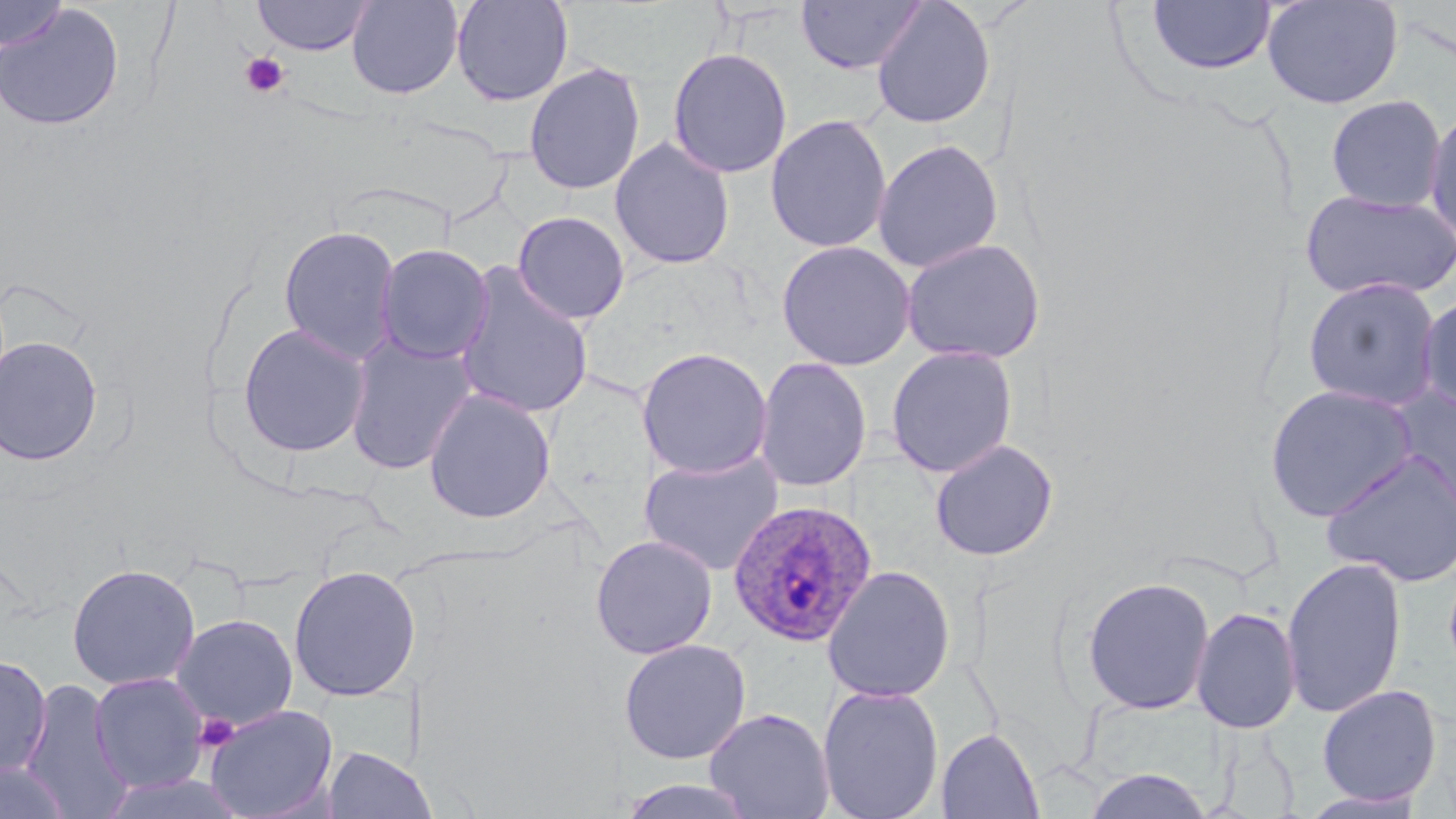
{
  "slide_level_diagnosis": "Plasmodium ovale",
  "stain": "May-Grünwald-Giemsa",
  "uninfected_red_blood_cell_locations": "approximate bounding boxes as (x1,y1)-(x2,y2) corner pairs in pixels: (0,0)-(68,52), (251,0)-(375,55), (346,0)-(464,100), (451,0)-(574,107), (795,0)-(927,75), (870,0)-(997,129), (1146,0)-(1277,76), (1261,0)-(1404,109), (0,2)-(125,132), (667,47)-(793,179), (523,62)-(646,196), (1325,94)-(1447,213), (1424,104)-(1456,247), (765,114)-(892,253), (609,137)-(735,271), (873,139)-(1004,273), (1299,188)-(1456,302), (512,211)-(630,325), (278,225)-(402,363), (900,237)-(1046,364), (776,240)-(916,371), (374,243)-(493,364), (452,265)-(596,420), (1302,276)-(1443,412), (1417,293)-(1456,419), (237,323)-(372,457), (344,333)-(478,476), (0,335)-(104,467), (885,344)-(1019,478), (636,346)-(773,480), (754,357)-(872,493), (1264,383)-(1420,523), (423,388)-(556,524), (1388,388)-(1456,518), (930,439)-(1058,561), (1319,448)-(1456,588), (638,450)-(784,576), (590,534)-(717,659), (1281,556)-(1407,719), (66,563)-(201,690), (288,564)-(421,702), (821,564)-(956,703), (1081,575)-(1215,715), (1191,606)-(1301,734), (172,613)-(299,731), (618,638)-(751,764), (0,655)-(52,779), (89,672)-(210,793), (20,678)-(134,819), (817,683)-(944,819), (1317,684)-(1441,807), (204,704)-(338,819), (705,707)-(834,819), (937,728)-(1044,819), (324,746)-(418,819), (0,758)-(72,819), (1083,768)-(1214,819), (616,778)-(761,819), (1300,789)-(1427,818)",
  "plasmodium_ovale_infected_red_blood_cell_locations": "approximate bounding boxes as (x1,y1)-(x2,y2) corner pairs in pixels: (728,500)-(878,646)",
  "modality": "optical microscopy",
  "magnification": "1000x",
  "image_size": "1456×819 pixels",
  "preparation": "thin blood film",
  "platelet_locations": "approximate bounding boxes as (x1,y1)-(x2,y2) corner pairs in pixels: (238,51)-(290,98), (194,713)-(239,752)",
  "field_of_view": "one of a larger specimen"
}